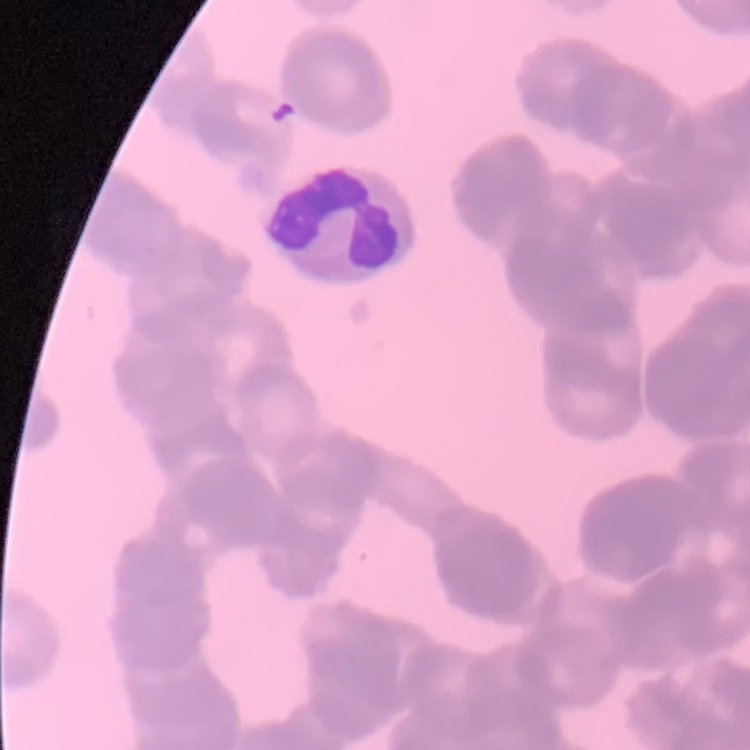 The red blood cells show rouleaux formation. One tile cut from a larger photomicrograph. Thin peripheral smear. Field's or Giemsa stain.